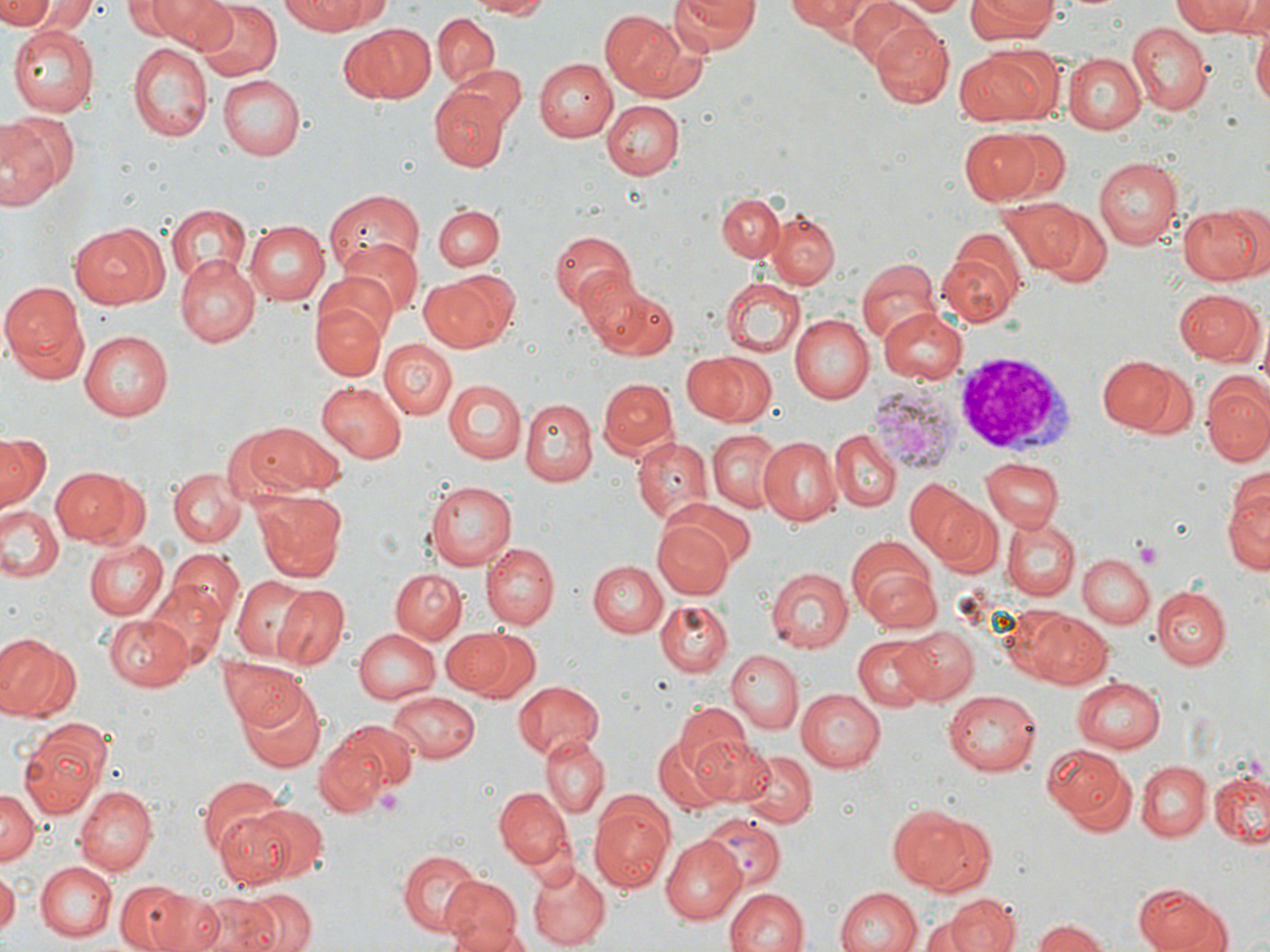 Approximate bounding boxes as [x1, y1, x2, y2] in pixels. Platelet locations: [1131, 538, 1164, 568], [373, 786, 405, 815]. Uninfected red blood cell locations: [0, 0, 55, 28], [19, 0, 95, 36], [124, 0, 193, 38], [144, 0, 234, 47], [194, 0, 281, 80], [282, 0, 387, 34], [463, 0, 552, 17], [669, 0, 758, 55], [790, 0, 876, 37], [895, 0, 969, 14], [965, 0, 1058, 43], [1172, 0, 1258, 36], [846, 1, 938, 73], [599, 10, 690, 99], [431, 14, 501, 90], [870, 21, 954, 104], [341, 24, 434, 103], [1124, 24, 1210, 114], [10, 27, 98, 116], [1251, 28, 1270, 116], [1072, 38, 1203, 129], [128, 41, 210, 142], [954, 46, 1056, 124], [1062, 52, 1146, 133], [534, 58, 618, 141], [456, 63, 526, 133], [217, 75, 304, 159], [429, 87, 507, 170], [601, 99, 683, 177], [0, 110, 78, 211], [1002, 129, 1073, 201], [961, 130, 1042, 204], [1093, 157, 1183, 248], [323, 188, 423, 272], [718, 194, 784, 261], [996, 197, 1086, 276], [723, 198, 829, 279], [1177, 203, 1266, 284], [167, 205, 250, 286], [434, 205, 503, 272], [1031, 206, 1111, 288], [767, 209, 840, 288], [247, 218, 331, 305], [69, 223, 166, 309], [548, 228, 638, 313], [333, 239, 423, 322], [937, 243, 1024, 330], [172, 256, 259, 344], [856, 266, 939, 348], [420, 271, 515, 353], [316, 274, 397, 346], [578, 275, 676, 359], [720, 278, 805, 358], [1, 280, 88, 380], [1173, 288, 1263, 365], [314, 302, 385, 380], [877, 306, 967, 383], [788, 313, 874, 404], [79, 330, 177, 421], [380, 339, 457, 418], [680, 352, 772, 426], [1098, 354, 1178, 432], [1123, 363, 1200, 443], [598, 376, 678, 460], [1203, 378, 1270, 466], [442, 379, 526, 464], [316, 382, 407, 462], [520, 399, 597, 485], [227, 420, 345, 502], [831, 429, 900, 511], [707, 430, 783, 514], [1, 433, 50, 513], [632, 437, 712, 527], [758, 437, 842, 525], [982, 459, 1062, 532], [1225, 464, 1268, 575], [51, 465, 142, 547], [168, 469, 246, 546], [423, 478, 517, 569], [905, 478, 986, 561], [251, 488, 348, 579], [661, 497, 756, 573], [935, 503, 1003, 577], [0, 505, 62, 584], [1002, 518, 1079, 601], [653, 520, 733, 599], [848, 536, 941, 628], [81, 539, 167, 620], [481, 542, 557, 629], [164, 546, 244, 631], [1078, 554, 1153, 629], [586, 560, 667, 637], [768, 565, 855, 652], [390, 570, 465, 643], [231, 576, 317, 659], [141, 581, 228, 669], [273, 585, 348, 670], [1152, 586, 1227, 670], [655, 600, 732, 677], [1027, 612, 1113, 689], [104, 614, 197, 692], [898, 627, 979, 703], [353, 628, 441, 705], [463, 628, 541, 705], [441, 630, 509, 694], [0, 633, 79, 722], [853, 636, 934, 712], [725, 650, 804, 734], [219, 658, 311, 730], [1071, 677, 1164, 753], [512, 678, 606, 759], [238, 684, 326, 773], [943, 688, 1042, 775], [795, 689, 884, 772], [386, 690, 480, 765], [674, 705, 750, 779], [17, 719, 113, 815], [327, 719, 417, 802], [653, 735, 733, 813], [540, 736, 608, 815], [691, 736, 777, 805], [314, 738, 387, 817], [1042, 744, 1134, 825], [743, 751, 815, 827], [1137, 760, 1211, 840], [1211, 769, 1269, 847], [199, 776, 289, 864], [74, 784, 158, 875], [0, 786, 40, 863], [494, 787, 572, 871], [589, 794, 674, 892], [243, 805, 328, 882], [891, 805, 989, 895], [212, 807, 297, 890], [703, 815, 785, 892], [658, 837, 748, 925], [396, 848, 482, 934], [35, 860, 116, 942], [527, 861, 610, 948], [0, 868, 18, 934], [440, 877, 523, 951], [117, 879, 208, 952], [1134, 883, 1225, 952], [835, 886, 921, 952], [237, 887, 317, 952], [724, 888, 809, 952], [190, 893, 284, 952], [945, 894, 1019, 952], [919, 917, 977, 951], [1033, 919, 1113, 952]. White blood cell locations: [949, 356, 1078, 460]. Plasmodium vivax-infected red blood cell locations: [868, 383, 962, 474]. Slide-level diagnosis: Plasmodium vivax. Optical microscopy. Thin blood smear. Image is 1270×952 pixels. May-Grünwald-Giemsa-stained preparation. One field of a larger specimen. Captured at 1000x magnification.